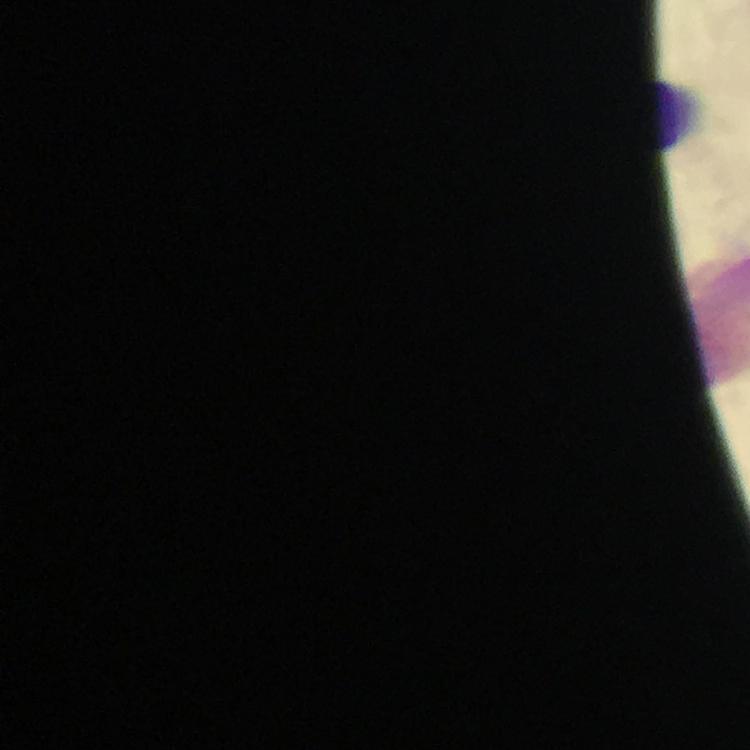 Approximate centers as [x, y] in pixels. Leukocyte locations: [679, 116]. Smartphone photograph taken through a microscope. A crop from one field of view. 100x magnification. Image is 750×750 pixels. From a diagnostic examination for malaria. Giemsa-stained preparation. Immersion oil was used. Thick blood smear. Malaria parasites: none seen.